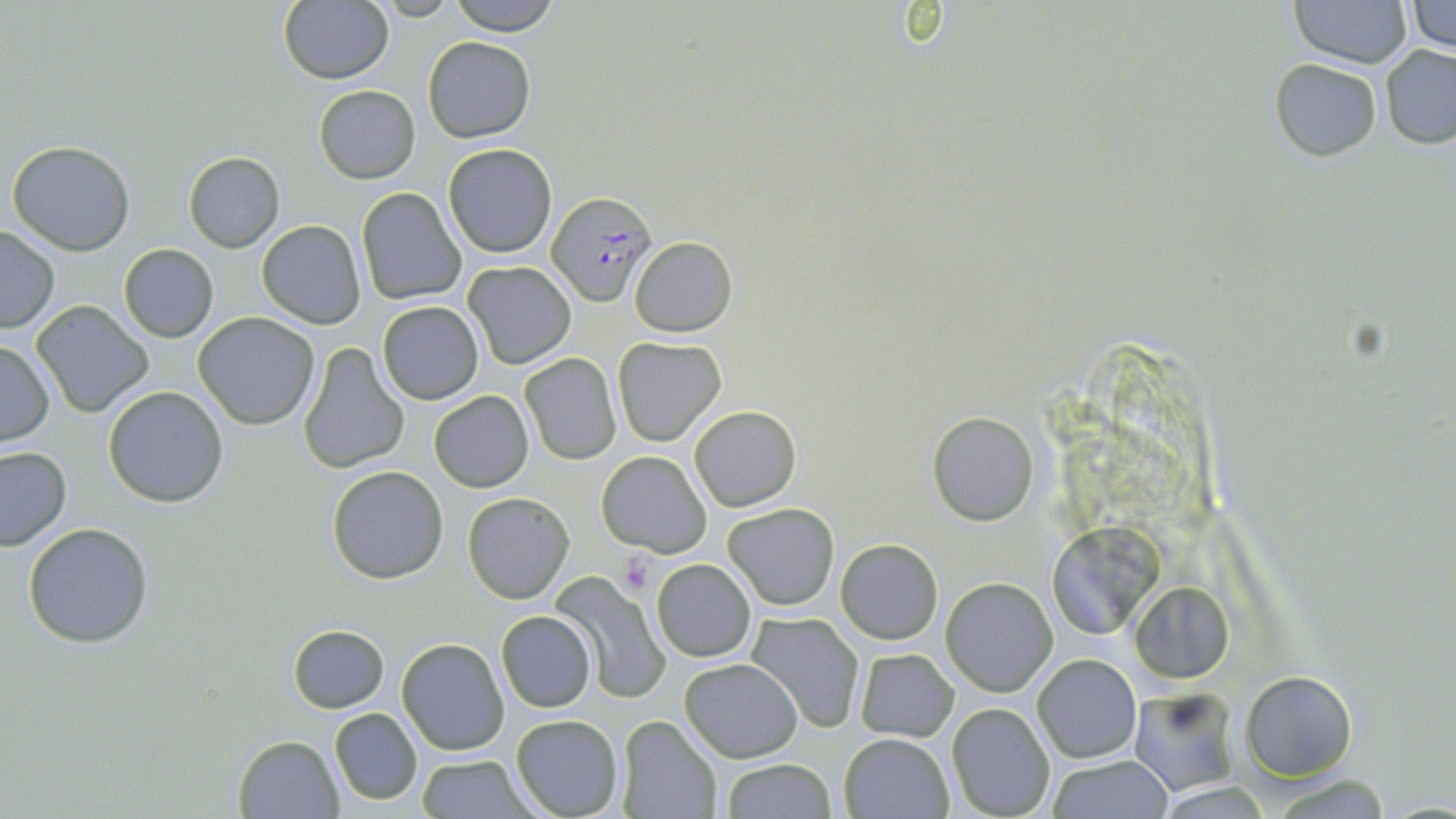
Summary:
  - Coordinate format: approximate bounding boxes as (x1,y1)-(x2,y2) corner pairs in pixels
  - Platelet locations: (620,553)-(657,593)
  - Plasmodium falciparum-infected red blood cell locations: (548,191)-(654,307)
  - Uninfected red blood cell locations: (448,0)-(562,35), (1289,0)-(1411,68), (279,2)-(392,84), (1406,2)-(1455,52), (423,36)-(536,144), (1380,45)-(1456,148), (1269,58)-(1382,161), (313,84)-(421,184), (7,140)-(135,254), (442,143)-(559,260), (183,152)-(284,253), (355,187)-(467,307), (257,220)-(367,329), (0,226)-(59,332), (630,236)-(738,336), (118,244)-(219,343), (462,261)-(577,368), (31,300)-(155,418), (376,301)-(485,404), (193,311)-(320,430), (611,337)-(727,448), (0,340)-(54,447), (297,341)-(410,475), (520,352)-(623,464), (103,385)-(229,507), (429,390)-(534,492), (689,405)-(801,512), (927,411)-(1040,526), (0,446)-(72,551), (597,451)-(711,557), (326,465)-(450,585), (463,491)-(574,603), (722,502)-(840,610), (24,522)-(153,647), (1044,524)-(1166,639), (836,539)-(943,644), (651,558)-(756,662), (552,571)-(669,702), (940,576)-(1059,696), (1130,581)-(1234,683), (496,610)-(598,713), (746,611)-(864,734), (288,624)-(389,713), (396,639)-(509,755), (854,648)-(959,742), (1031,653)-(1143,763), (679,657)-(801,762), (1241,671)-(1357,780), (1128,687)-(1241,795), (947,702)-(1056,819), (331,708)-(423,807), (511,714)-(625,819), (616,717)-(721,818), (838,732)-(953,818), (232,734)-(343,818), (415,754)-(536,818), (1046,755)-(1174,819), (719,759)-(837,818), (1269,774)-(1397,817), (1153,782)-(1277,817)
  - Slide-level diagnosis: Plasmodium falciparum
  - Modality: light microscopy
  - Stain: May-Grünwald-Giemsa
  - Preparation: thin blood film
  - Magnification: 1000x
  - Field of view: one of a larger specimen
  - Image size: 1456×819 pixels